State which cell type is depicted.
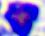

A leukocyte.

Summary:
  - Modality: micrograph
  - Magnification: 400x